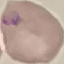

Summary:
  - Malaria status: parasitized
  - Stain: Giemsa
  - Preparation: thin blood film
  - Capture: smartphone camera at the microscope eyepiece
  - Image type: cell patch, automatically extracted from a larger field of view and resized to 64 × 64 pixels